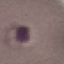 Result: no malaria parasites seen. Thin blood film. Acquired by smartphone through the microscope eyepiece. Giemsa stain. Cell patch, automatically extracted from a larger field of view and resized to 64 × 64 pixels.